Describe the morphology of the erythrocytes.
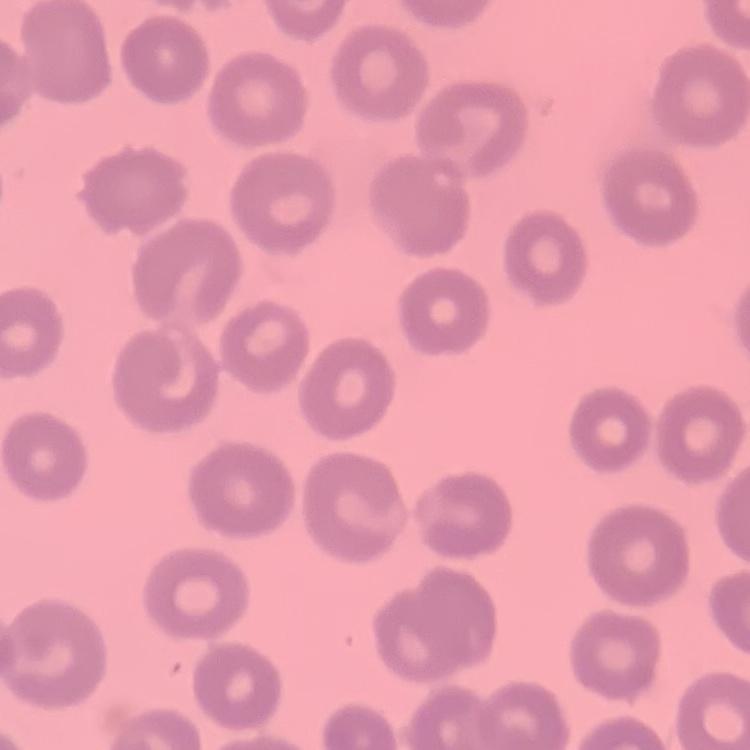

No rouleaux formation.

{
  "image_type": "square crop of a larger photomicrograph",
  "stain": "Field's or Giemsa",
  "preparation": "thin peripheral smear"
}